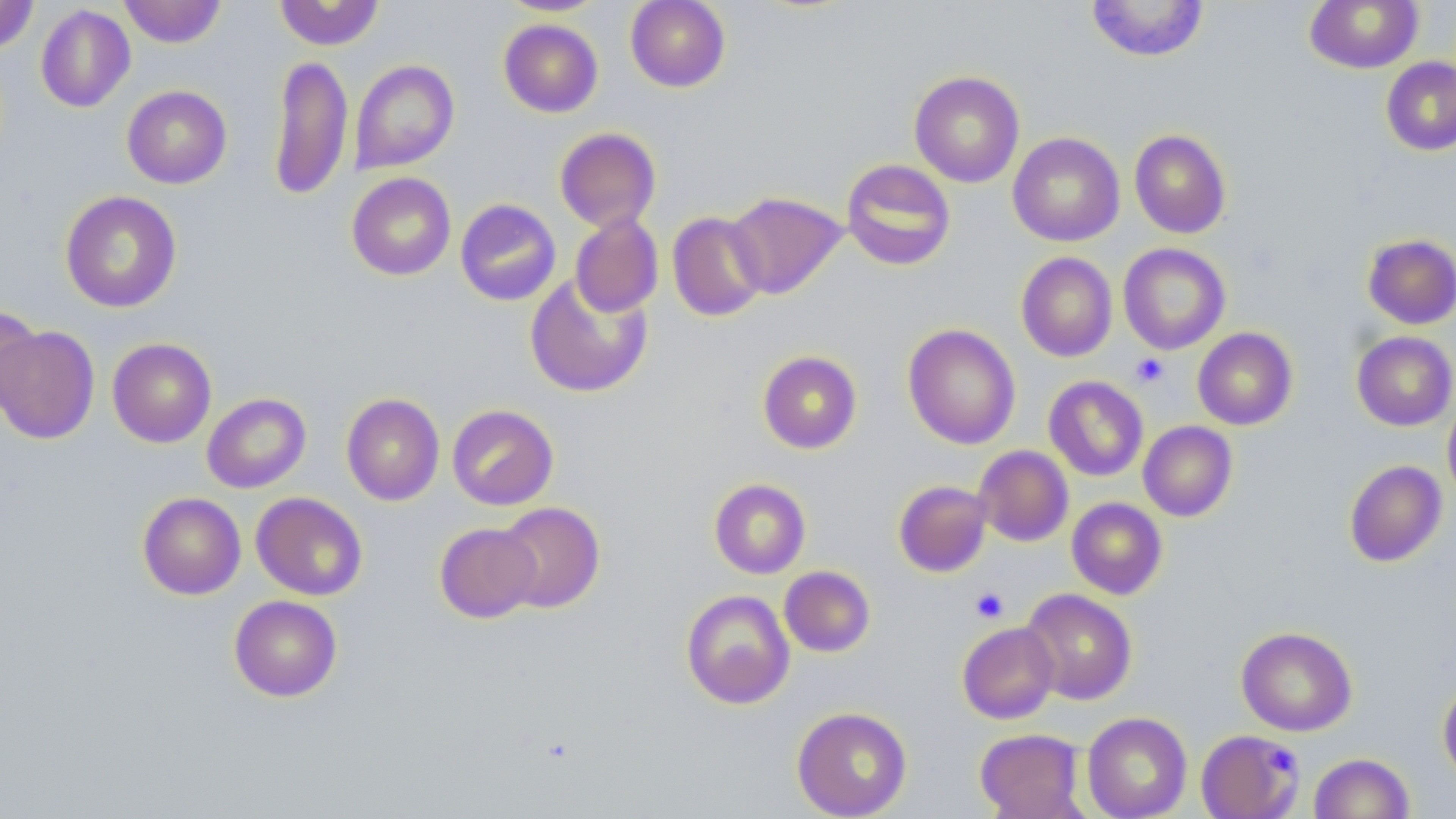

Approximate bounding boxes as [x1, y1, x2, y2] in pixels. Uninfected red blood cell locations: [0, 0, 39, 53], [118, 0, 227, 47], [274, 0, 385, 50], [495, 0, 609, 16], [625, 0, 731, 92], [1085, 0, 1210, 62], [1304, 1, 1423, 73], [35, 4, 136, 113], [498, 19, 603, 118], [268, 55, 353, 201], [1381, 57, 1456, 156], [350, 59, 459, 174], [909, 70, 1025, 188], [122, 85, 232, 189], [555, 127, 661, 232], [1129, 130, 1231, 238], [1007, 132, 1125, 247], [841, 159, 956, 271], [346, 172, 456, 280], [60, 190, 182, 312], [725, 191, 847, 299], [455, 199, 561, 306], [667, 211, 769, 322], [570, 212, 664, 318], [1362, 234, 1456, 329], [1118, 243, 1231, 354], [1016, 252, 1117, 362], [524, 272, 653, 398], [1, 305, 43, 419], [902, 323, 1021, 449], [1, 325, 100, 445], [1192, 327, 1298, 430], [1352, 331, 1456, 431], [107, 338, 216, 447], [757, 350, 862, 454], [1043, 376, 1149, 481], [202, 392, 311, 493], [341, 393, 445, 506], [1443, 396, 1456, 504], [447, 404, 559, 510], [1138, 421, 1238, 521], [973, 445, 1074, 547], [1344, 460, 1447, 567], [709, 478, 811, 578], [893, 480, 992, 577], [137, 492, 246, 599], [251, 492, 368, 600], [1067, 497, 1168, 599], [495, 502, 605, 612], [434, 522, 542, 623], [779, 566, 876, 657], [1020, 588, 1137, 705], [680, 589, 795, 709], [229, 595, 342, 702], [957, 622, 1060, 724], [1236, 626, 1358, 736], [1438, 678, 1456, 783], [791, 706, 912, 818], [1081, 711, 1193, 819], [974, 728, 1086, 818], [1196, 729, 1306, 818], [1309, 753, 1415, 818]. Platelet locations: [1131, 353, 1169, 388], [970, 587, 1009, 623], [1267, 743, 1294, 776]. Slide-level diagnosis: negative for blood parasites. Optical microscopy. May-Grünwald-Giemsa-stained preparation. Captured at 1000x magnification. One field of a larger specimen. Image is 1456×819 pixels. Thin blood film.